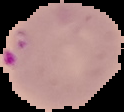
preparation = thin blood film
image type = segmented cell region on a black background
malaria status = parasitized
image size = 124×112 pixels